Give the position of every malaria parasite.
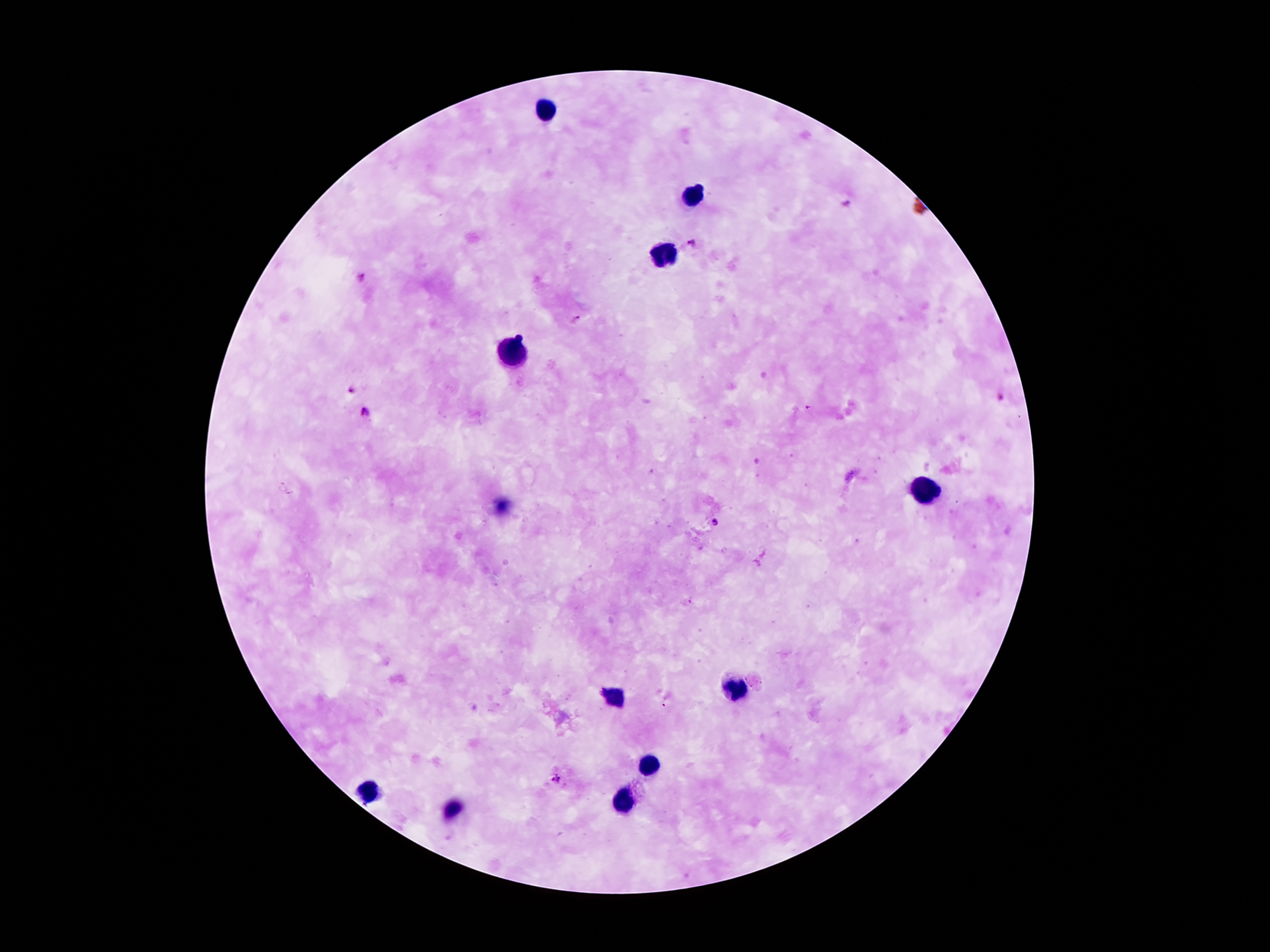

Approximate centers as (x, y) in pixels.
Malaria parasites: (848, 203), (689, 244), (361, 278), (578, 321), (350, 390), (808, 407), (364, 413), (714, 524), (556, 779).

Summary:
  - Leukocyte locations: (545, 113), (689, 199), (662, 256), (516, 354), (923, 493), (734, 689), (611, 697), (650, 762), (368, 791), (629, 802), (452, 811)
  - Capture: smartphone through the microscope eyepiece
  - Magnification: 100x
  - Image size: 1270×952 pixels
  - Field of view: one from this slide
  - Preparation: thick blood film
  - Patient malaria status: infected with Plasmodium falciparum
  - Stain: Giemsa